Point out each leukocyte.
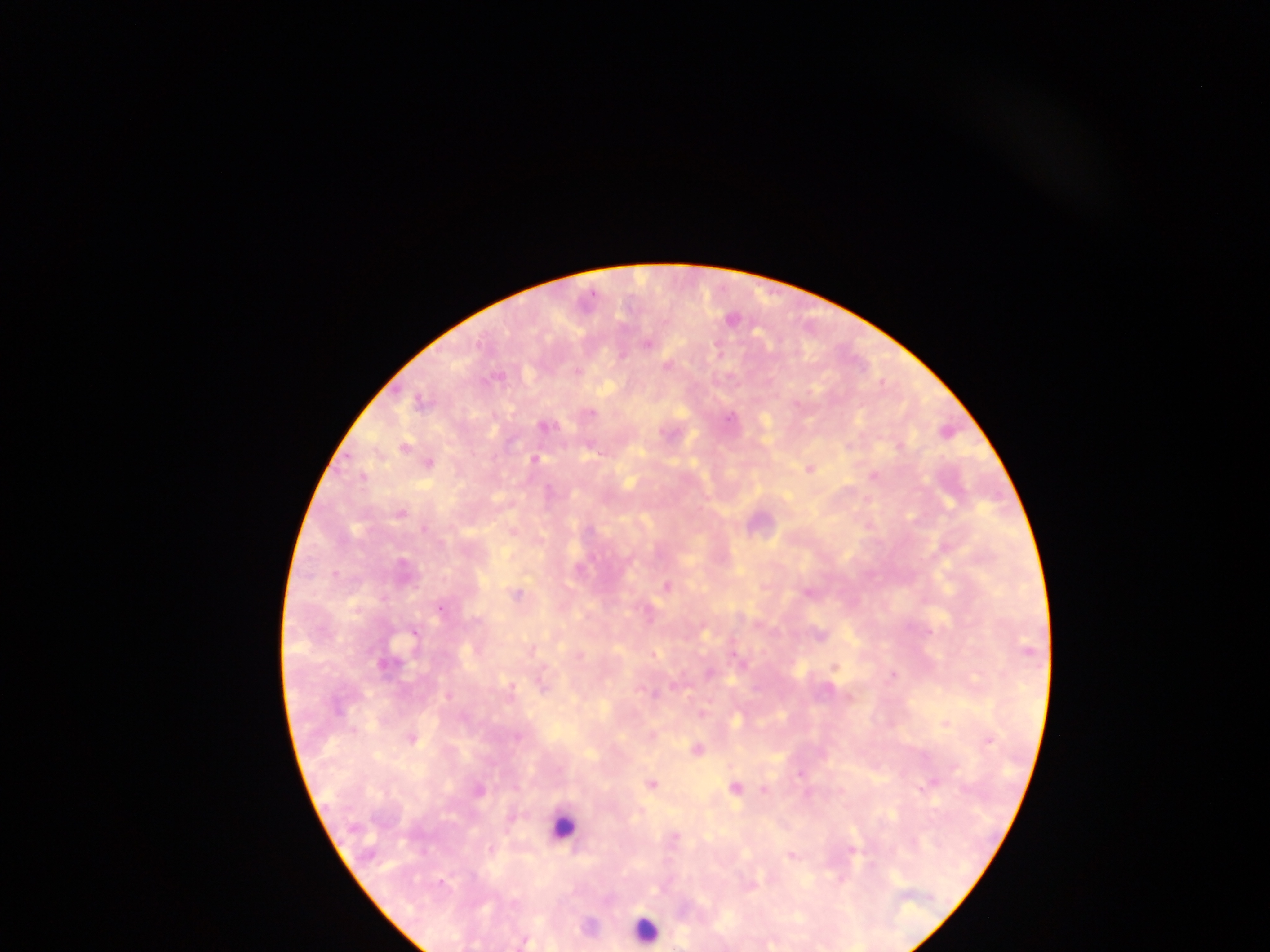

Approximate centers as (x, y) in pixels.
Leukocytes: (564, 829), (652, 928).

Plasmodium parasite locations: (730, 320), (647, 344), (717, 348), (623, 355), (666, 366), (574, 371), (590, 414), (728, 419), (761, 426), (547, 427), (534, 459), (807, 469), (870, 476), (400, 513), (913, 517), (425, 528), (668, 585), (809, 591), (517, 594), (754, 624), (703, 633), (818, 634), (531, 650), (578, 657), (833, 667), (892, 675), (543, 684), (673, 684), (509, 689), (448, 696), (848, 697), (701, 709), (738, 719), (944, 724), (651, 736), (518, 737), (411, 739), (989, 742), (696, 750), (798, 776), (930, 779), (651, 784), (734, 788), (763, 790), (479, 791), (917, 791), (808, 795), (675, 837), (489, 848), (851, 851), (789, 854), (752, 883), (587, 927), (526, 941). Mobile-phone photograph taken through the microscope. Thick blood smear. Sample from Ghana. Image is 1270×952 pixels. One field of view.